Assess this cell for malaria.
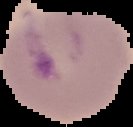

Uninfected.

The area outside the segmented cell region is set to black. Image is 133×127 pixels. From a thin blood smear.